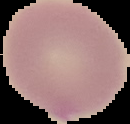
Result: negative for Plasmodium parasites. Image is 130×124 pixels. From a thin blood smear. The area outside the segmented cell region is set to black.